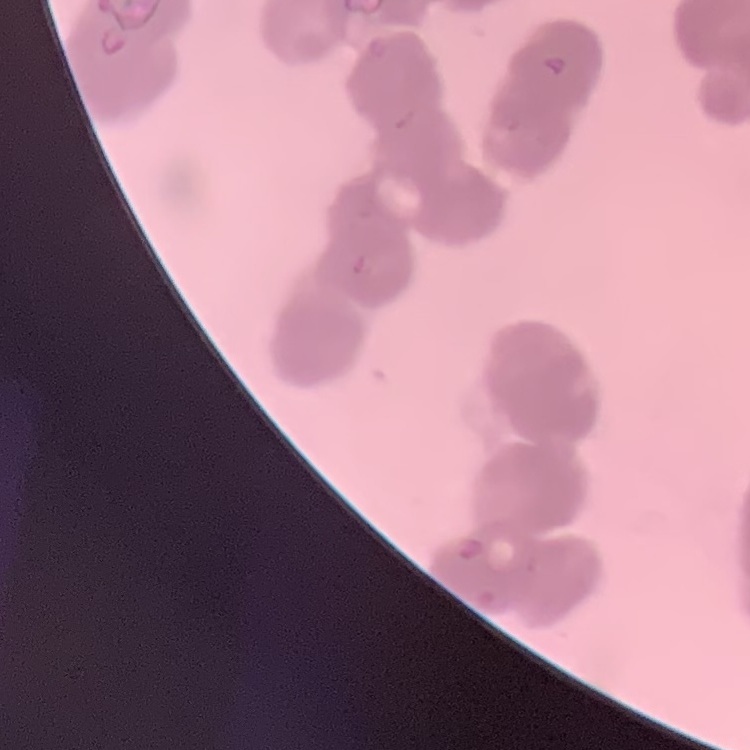
Summary:
  - Red blood cell morphology: rouleaux formation
  - Image type: one tile cut from a larger photomicrograph
  - Stain: Field's or Giemsa
  - Preparation: thin peripheral smear